Classify this cell by malaria status.
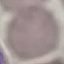
Uninfected.

Acquired by smartphone through the microscope eyepiece. Automatically extracted cell patch, resized to 64 × 64 pixels. Thin smear of blood. Giemsa-stained preparation.